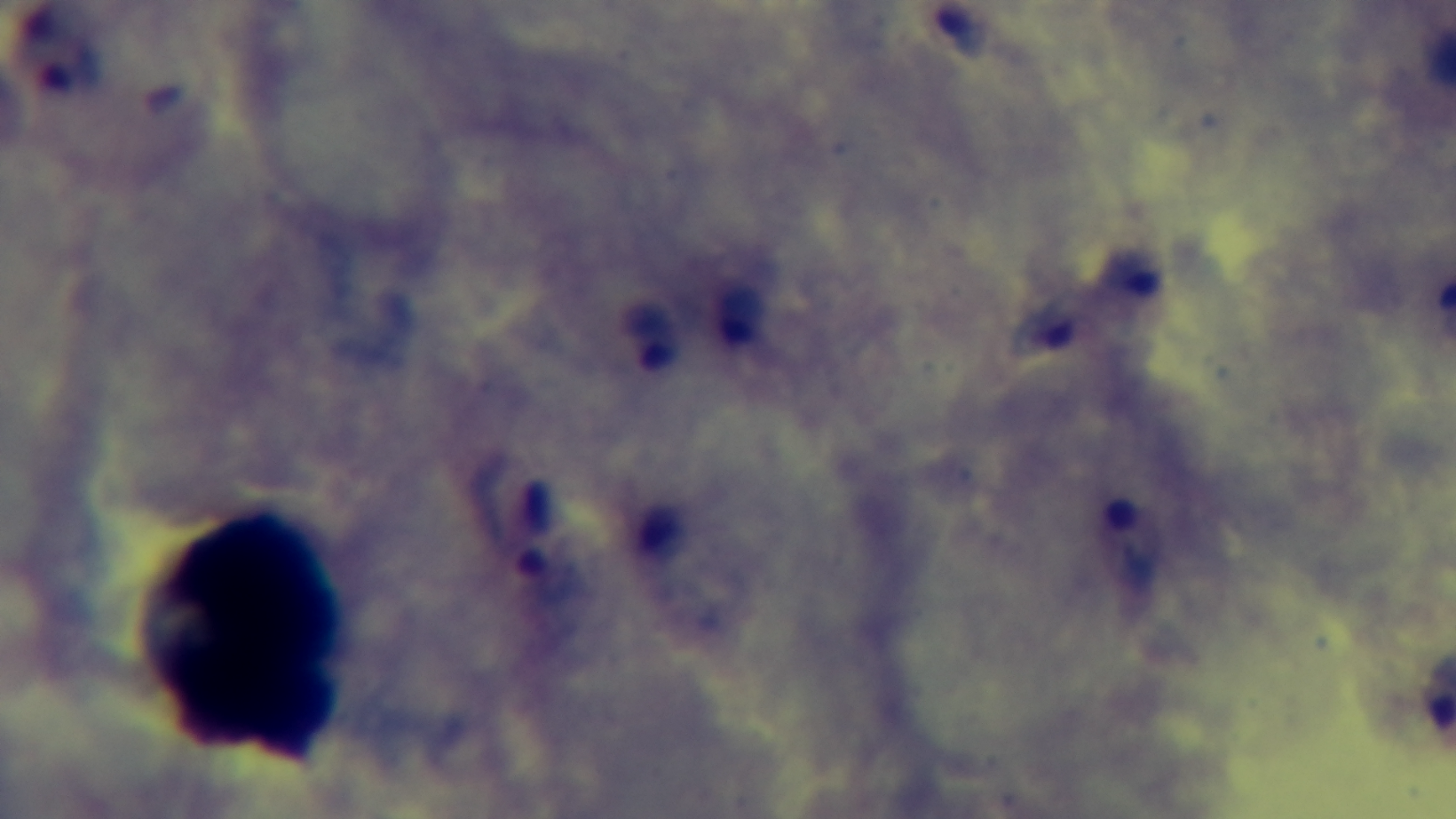
preparation = thick
malaria status = positive
objective = 100x oil immersion
stain = Giemsa
field of view = single
modality = light microscopy
capture = mounted 4K digital camera